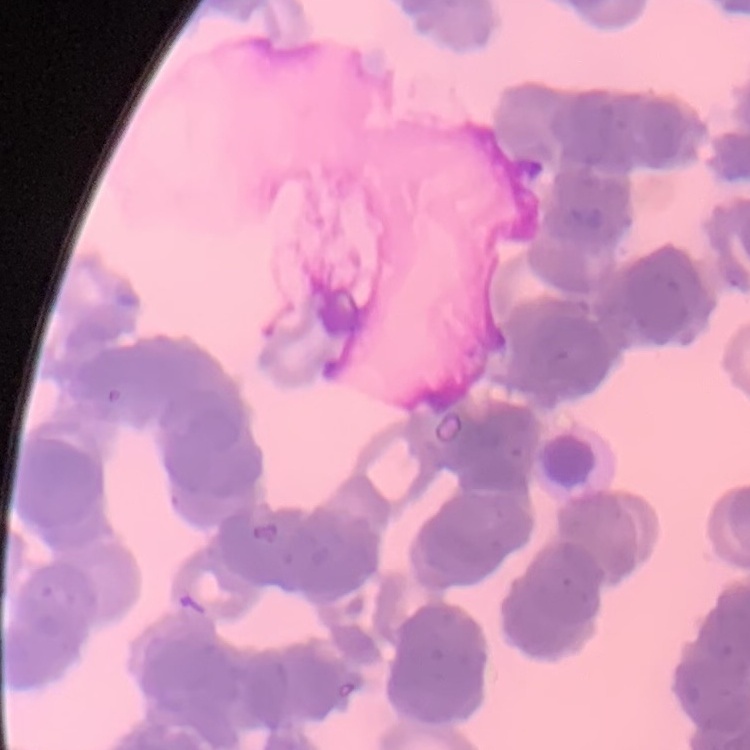

The red blood cells exhibit rouleaux formation. Square crop of a larger photomicrograph. Field's or Giemsa stain. Thin peripheral smear.